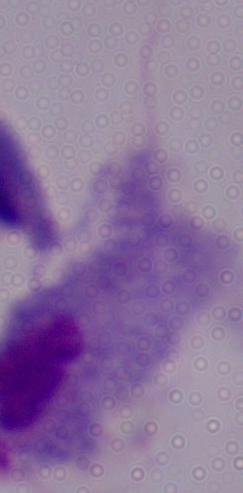
magnification = 1000x
modality = micrograph
identification = trichomonad